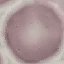

Summary:
  - Malaria status: uninfected
  - Preparation: thin blood smear
  - Capture: smartphone through the microscope eyepiece
  - Image type: cell patch, automatically extracted from a larger field of view and resized to 64 × 64 pixels
  - Stain: Giemsa